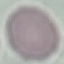
malaria status = uninfected
capture = smartphone camera at the microscope eyepiece
image type = cell patch, automatically extracted from a larger field of view and resized to 64 × 64 pixels
preparation = thin blood smear
stain = Giemsa